Comment on the morphology of the red blood cells.
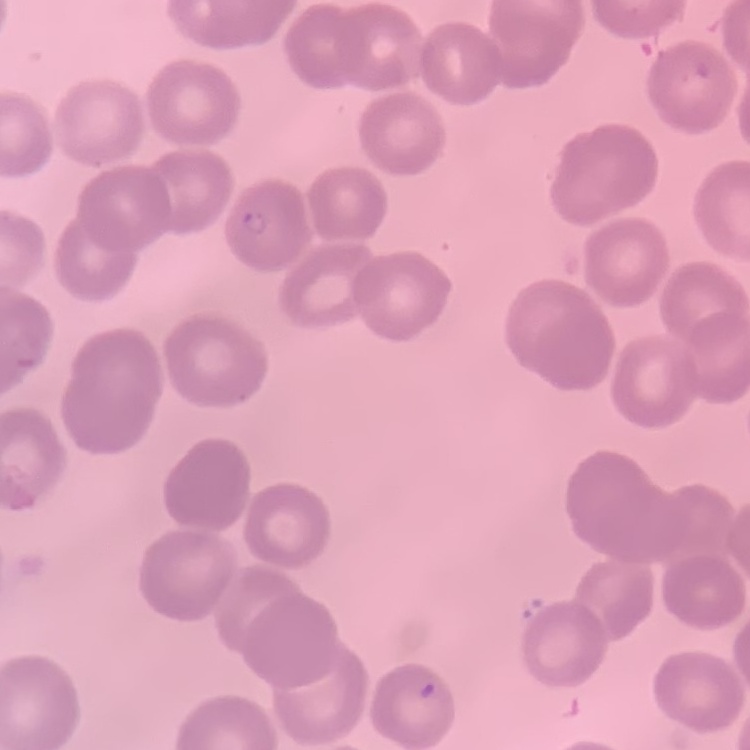

They show no rouleaux formation.

stain = Field's or Giemsa
image type = one tile cut from a larger photomicrograph
preparation = thin blood smear